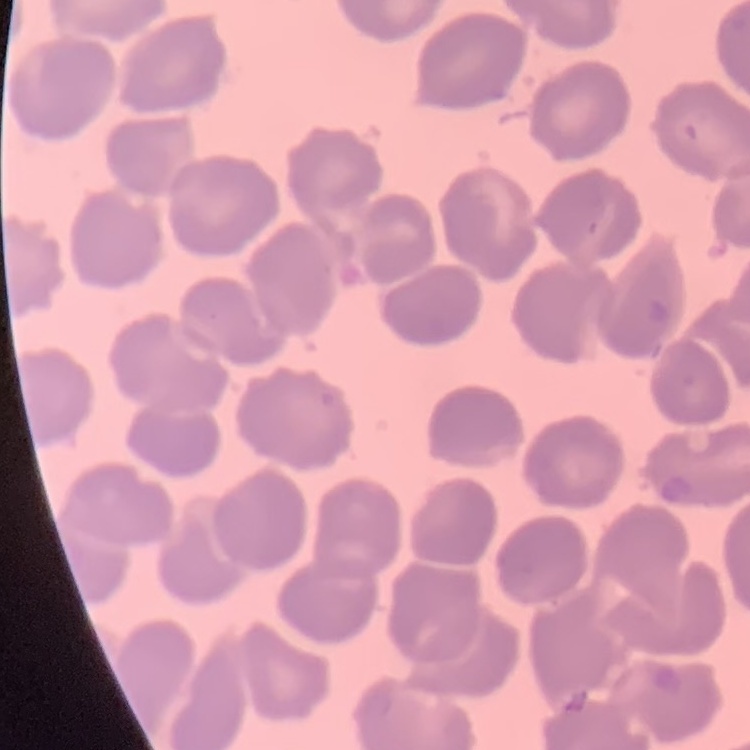
Summary:
  - Erythrocyte morphology: no rouleaux formation
  - Preparation: thin blood film
  - Image type: square crop of a larger photomicrograph
  - Stain: Field's or Giemsa